Outline each blood parasite and name the species.
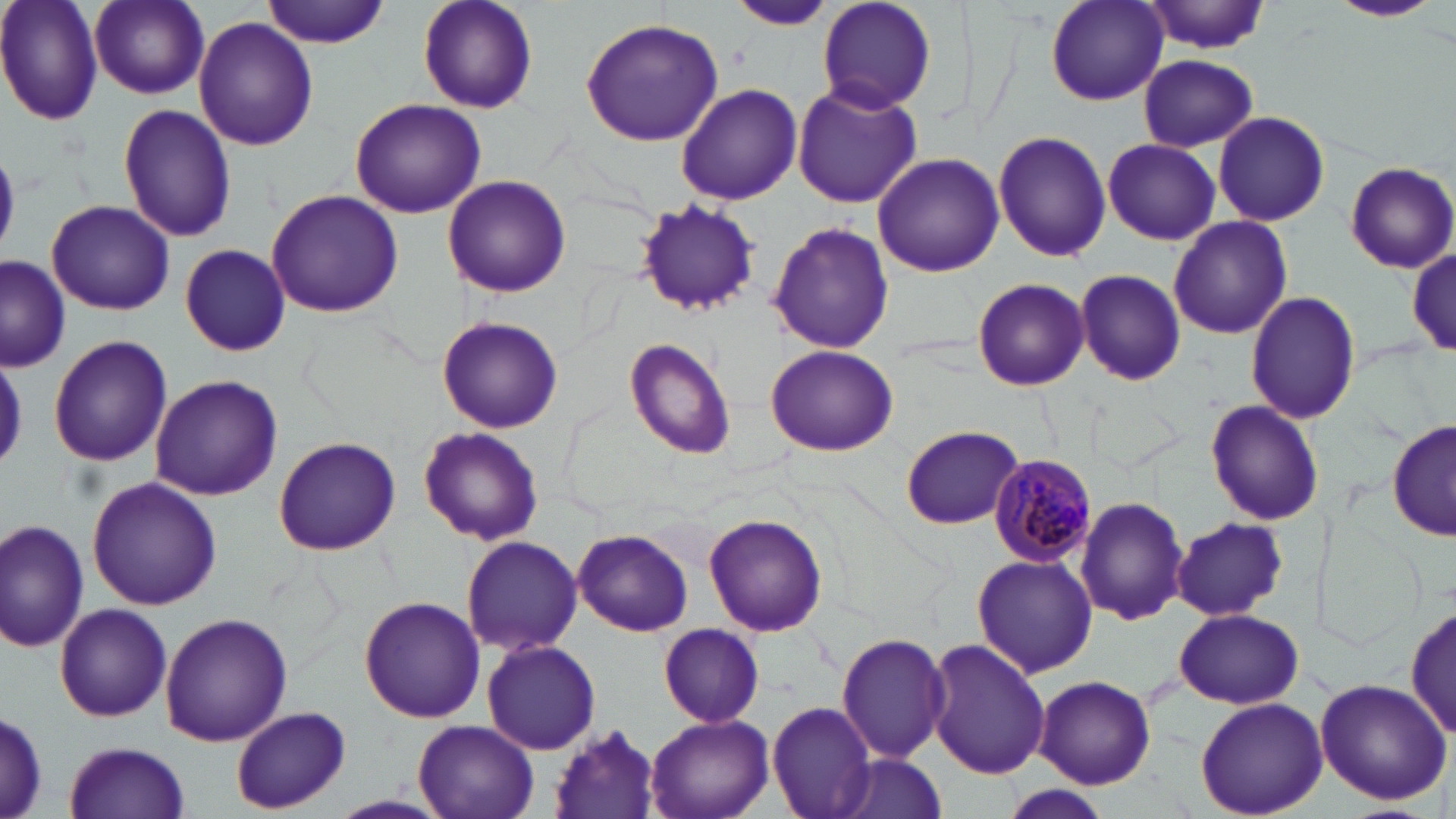
Approximate bounding boxes as [x1, y1, x2, y2] in pixels.
Plasmodium malariae-infected red blood cells: [986, 452, 1097, 566].
No Plasmodium falciparum, Plasmodium ovale, Plasmodium vivax, Babesia divergens, or Trypanosoma brucei observed.

slide-level diagnosis = Plasmodium malariae
magnification = 1000x
stain = May-Grünwald-Giemsa
preparation = thin blood film
modality = light microscopy
image size = 1456×819 pixels
field of view = one of a larger specimen
uninfected red blood cell locations = approximate bounding boxes as [x1, y1, x2, y2] in pixels: [0, 0, 103, 125], [89, 0, 210, 100], [262, 0, 392, 48], [416, 0, 539, 114], [814, 0, 939, 115], [1043, 0, 1168, 105], [1330, 0, 1441, 22], [727, 3, 839, 31], [1143, 3, 1274, 55], [194, 18, 317, 150], [580, 18, 724, 145], [1137, 53, 1256, 151], [676, 83, 802, 206], [794, 84, 921, 209], [349, 98, 486, 218], [117, 102, 237, 242], [1212, 109, 1331, 226], [993, 130, 1110, 263], [1100, 140, 1220, 245], [872, 153, 1003, 277], [1340, 160, 1456, 274], [444, 175, 569, 296], [265, 188, 405, 318], [46, 200, 175, 316], [631, 201, 764, 314], [1168, 214, 1292, 340], [768, 222, 894, 354], [180, 244, 292, 355], [1407, 248, 1455, 358], [0, 255, 71, 371], [1074, 272, 1187, 386], [972, 278, 1090, 391], [1245, 289, 1361, 426], [437, 315, 563, 433], [47, 335, 174, 467], [624, 337, 737, 460], [765, 344, 897, 456], [149, 375, 285, 500], [1205, 398, 1323, 527], [1387, 418, 1456, 541], [901, 425, 1024, 530], [418, 426, 544, 545], [273, 436, 402, 555], [86, 476, 223, 610], [1078, 496, 1189, 624], [704, 513, 828, 638], [1172, 517, 1287, 620], [0, 519, 89, 655], [573, 528, 693, 636], [459, 534, 584, 655], [972, 553, 1098, 680], [360, 596, 486, 722], [1407, 603, 1456, 741], [55, 604, 173, 722], [1173, 608, 1303, 708], [159, 612, 292, 745], [656, 622, 766, 727], [836, 632, 952, 763], [480, 637, 601, 755], [924, 638, 1051, 779], [1033, 675, 1155, 788], [1313, 676, 1452, 806], [1195, 697, 1327, 818], [767, 701, 877, 818], [232, 706, 350, 814], [1, 709, 48, 817], [644, 712, 776, 819], [413, 720, 538, 819], [547, 726, 664, 818], [62, 741, 193, 818], [830, 753, 947, 819], [998, 785, 1116, 819], [331, 793, 454, 817]